Assess the morphology of the red blood cells.
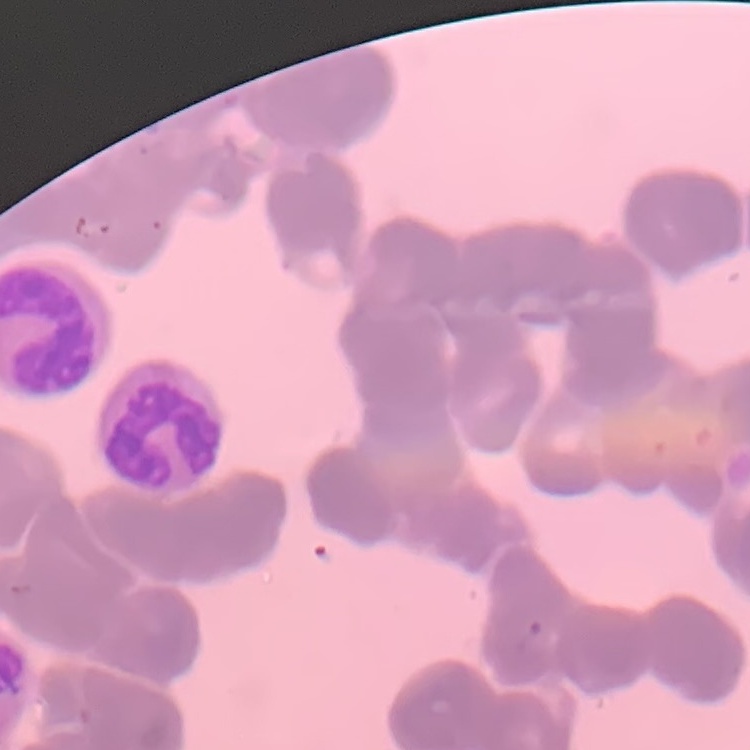
They show rouleaux formation.

Summary:
  - Stain: Field's or Giemsa
  - Image type: square crop of a larger photomicrograph
  - Preparation: thin peripheral smear